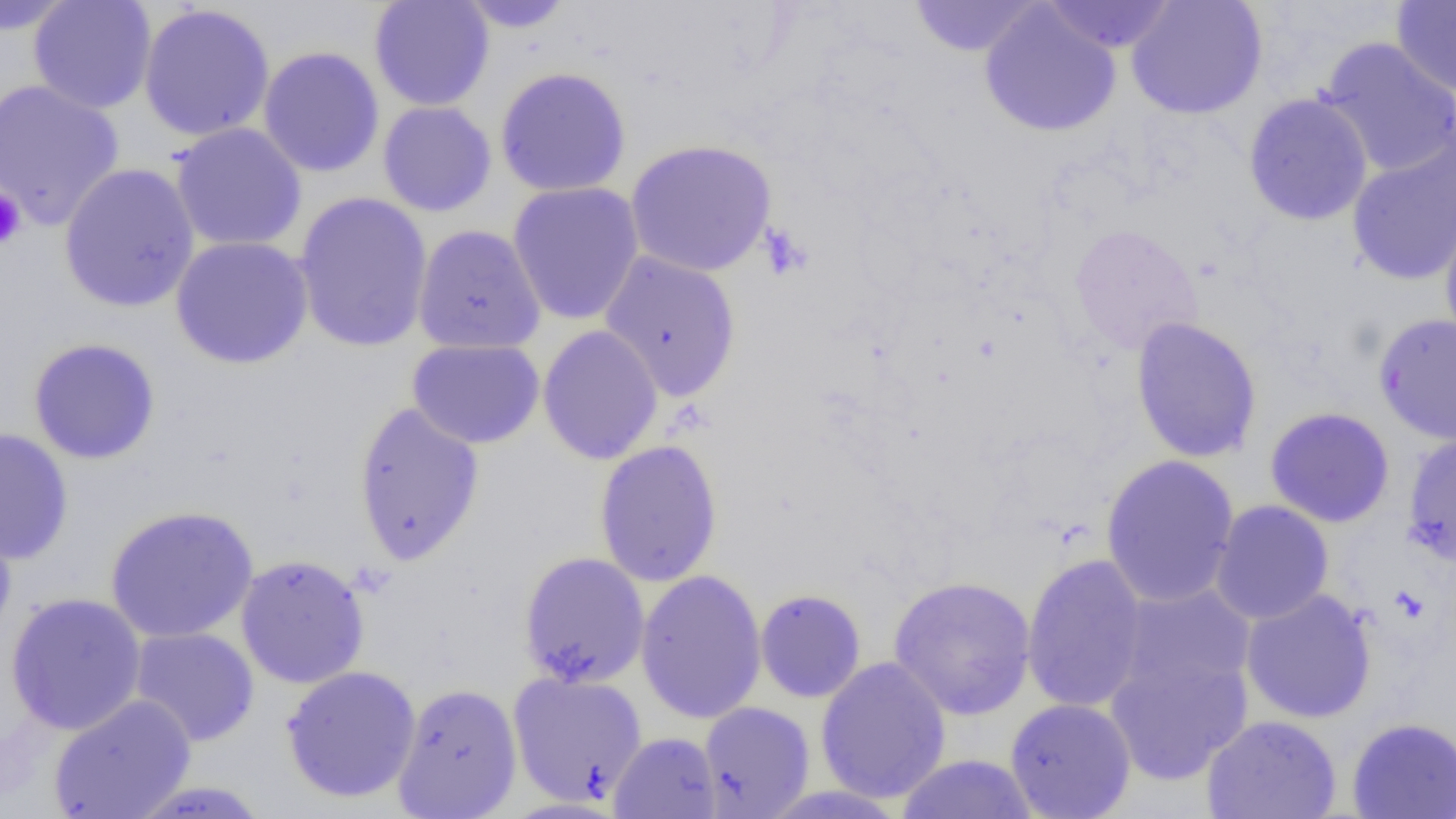 Approximate bounding boxes as (x1, y1, x2, y2) in pixels. Uninfected red blood cell locations: (0, 0, 78, 35), (28, 0, 157, 114), (908, 0, 1042, 57), (1041, 0, 1176, 54), (1126, 0, 1268, 120), (369, 1, 495, 111), (456, 1, 576, 32), (1391, 1, 1455, 97), (979, 3, 1121, 138), (137, 4, 276, 142), (1317, 36, 1456, 178), (258, 46, 385, 178), (494, 67, 631, 197), (0, 79, 125, 230), (1243, 93, 1373, 226), (377, 101, 497, 217), (170, 123, 308, 252), (1346, 135, 1456, 286), (625, 139, 778, 277), (58, 162, 200, 313), (507, 181, 645, 325), (293, 192, 433, 353), (1439, 198, 1456, 351), (412, 224, 546, 355), (1068, 224, 1203, 355), (170, 236, 314, 369), (599, 251, 742, 403), (1373, 312, 1456, 445), (1130, 316, 1262, 463), (537, 324, 664, 465), (27, 337, 161, 464), (407, 338, 545, 449), (352, 400, 485, 567), (1264, 407, 1395, 528), (0, 427, 74, 565), (1402, 431, 1456, 567), (593, 439, 723, 588), (1100, 454, 1240, 608), (1209, 500, 1334, 624), (104, 505, 259, 643), (0, 510, 17, 646), (519, 551, 650, 688), (1021, 552, 1149, 713), (235, 554, 370, 689), (635, 569, 767, 725), (888, 575, 1037, 721), (1114, 583, 1257, 703), (1239, 588, 1377, 724), (755, 589, 867, 703), (5, 592, 147, 735), (129, 626, 260, 747), (1104, 647, 1253, 786), (815, 656, 952, 804), (281, 665, 421, 803), (507, 671, 648, 806), (392, 682, 522, 819), (48, 694, 196, 819), (1004, 697, 1137, 818), (698, 701, 815, 818), (1201, 714, 1341, 819), (1347, 716, 1456, 818), (608, 731, 722, 819), (895, 753, 1039, 818), (127, 781, 274, 818). Platelet locations: (0, 188, 27, 251), (757, 223, 813, 281). Slide-level diagnosis: negative for blood parasites. Light microscopy. Captured at 1000x magnification. Thin blood film. Single field of view. Image is 1456×819 pixels.